Assess the morphology of the erythrocytes.
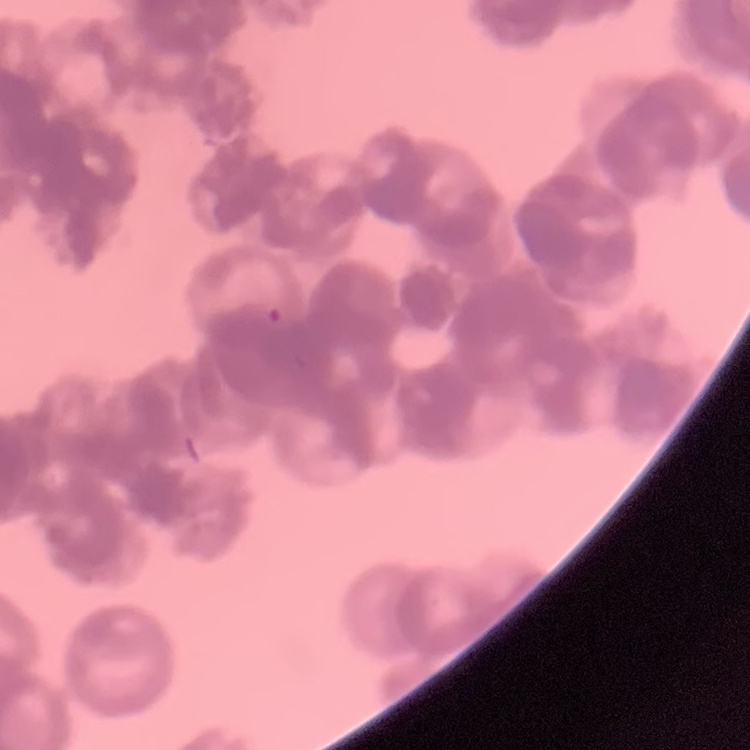

Rouleaux formation.

Summary:
  - Stain: Field's or Giemsa
  - Image type: square crop of a larger photomicrograph
  - Preparation: thin blood smear